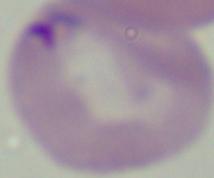
Summary:
  - Identification: Babesia
  - Modality: micrograph
  - Magnification: 1000x